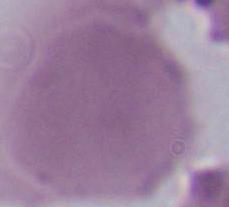

A red blood cell is seen. Photomicrograph. 1000x magnification.